Describe the morphology of the erythrocytes.
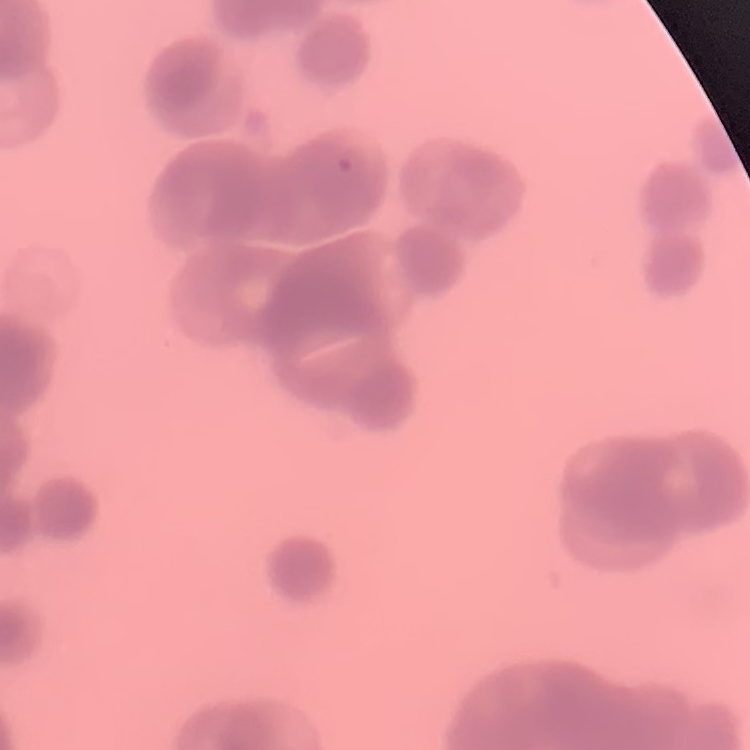
Rouleaux formation.

Field's or Giemsa stain. Thin peripheral smear. Square crop of a larger photomicrograph.